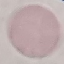

Summary:
  - Malaria status: uninfected
  - Preparation: thin blood film
  - Capture: smartphone through the microscope eyepiece
  - Stain: Giemsa
  - Image type: cell patch, automatically extracted from a larger field of view and resized to 64 × 64 pixels